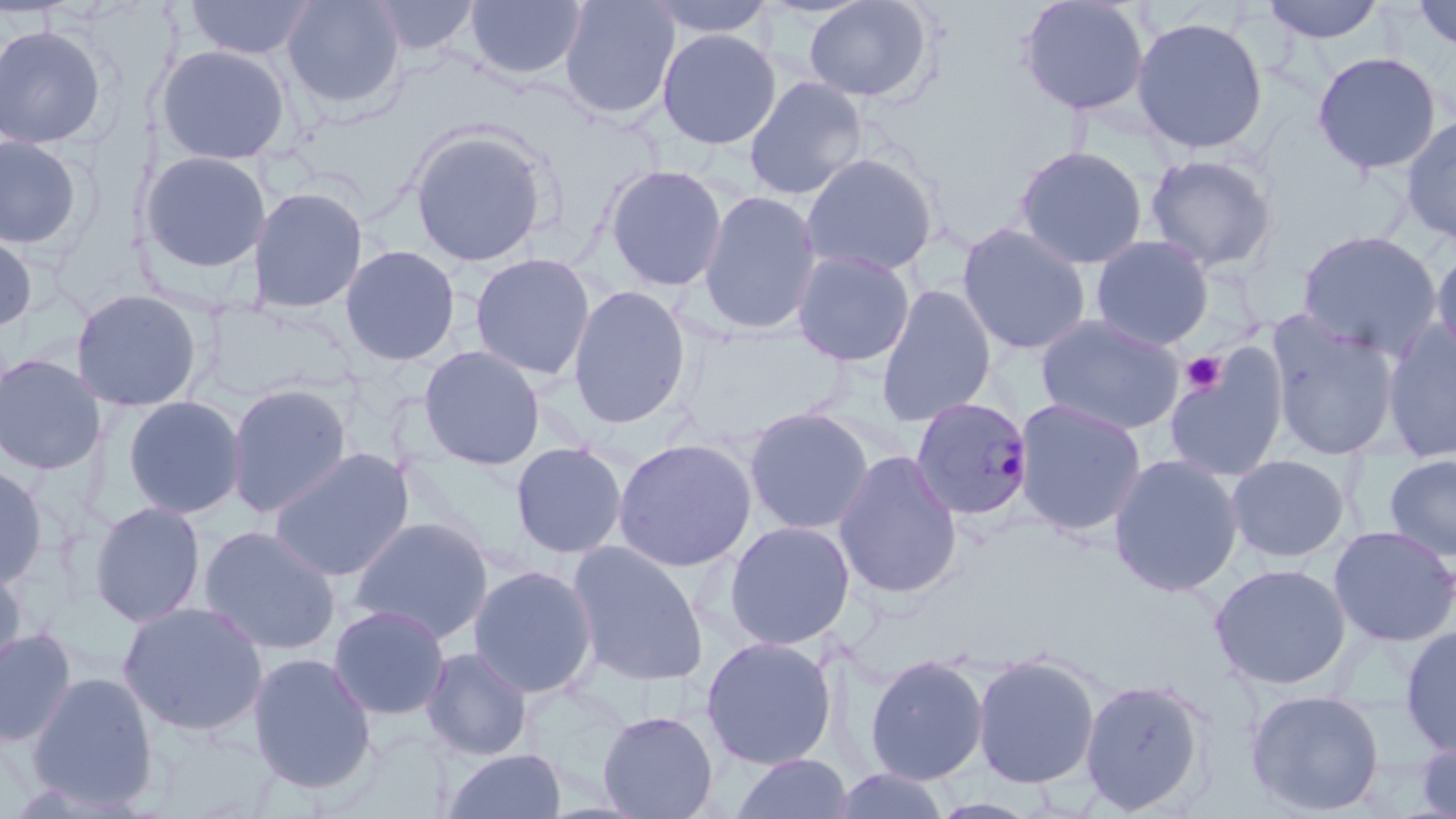
Summary:
  - Coordinate format: approximate bounding boxes as [x1, y1, x2, y2] in pixels
  - Platelet locations: [1181, 351, 1227, 395]
  - Plasmodium malariae-infected red blood cell locations: [910, 396, 1034, 521]
  - Uninfected red blood cell locations: [183, 0, 317, 60], [368, 0, 480, 56], [559, 0, 680, 120], [643, 0, 777, 39], [804, 0, 932, 103], [1018, 0, 1150, 116], [1261, 0, 1385, 44], [1412, 0, 1456, 53], [282, 1, 404, 110], [465, 1, 587, 81], [1131, 16, 1269, 154], [1, 24, 108, 149], [657, 28, 781, 149], [156, 44, 292, 165], [1312, 51, 1442, 174], [744, 76, 867, 200], [1400, 115, 1456, 247], [410, 128, 550, 267], [0, 135, 83, 250], [1014, 145, 1148, 270], [138, 150, 271, 274], [800, 153, 938, 277], [1145, 153, 1278, 273], [604, 164, 728, 291], [248, 185, 368, 314], [699, 191, 821, 335], [956, 223, 1092, 355], [1297, 230, 1442, 360], [0, 232, 37, 333], [1091, 235, 1213, 350], [1431, 243, 1456, 363], [339, 244, 461, 366], [792, 249, 916, 366], [469, 253, 596, 380], [876, 284, 996, 426], [568, 285, 691, 429], [71, 289, 205, 412], [1035, 314, 1185, 436], [1266, 314, 1401, 461], [1382, 322, 1456, 463], [1164, 343, 1289, 483], [419, 345, 545, 470], [0, 353, 105, 475], [226, 383, 352, 517], [122, 395, 247, 519], [1013, 398, 1147, 536], [744, 407, 874, 535], [613, 437, 757, 572], [510, 441, 628, 560], [268, 447, 415, 582], [833, 449, 963, 598], [1108, 453, 1244, 596], [1226, 454, 1350, 562], [1383, 454, 1456, 562], [0, 462, 48, 590], [89, 501, 206, 626], [348, 516, 495, 645], [724, 521, 855, 650], [198, 525, 341, 655], [1328, 525, 1456, 647], [567, 541, 708, 687], [1210, 563, 1351, 689], [0, 564, 27, 682], [467, 564, 599, 699], [117, 600, 269, 736], [327, 604, 450, 720], [1399, 625, 1456, 757], [0, 627, 77, 747], [700, 636, 837, 770], [421, 647, 532, 761], [247, 651, 377, 794], [971, 652, 1101, 789], [864, 653, 988, 785], [26, 672, 159, 809], [1079, 677, 1209, 815], [1244, 689, 1385, 816], [597, 709, 719, 819], [1416, 735, 1456, 819], [441, 748, 567, 819], [729, 753, 854, 818], [830, 768, 952, 819], [929, 796, 1045, 818]
  - Slide-level diagnosis: Plasmodium malariae
  - Modality: optical microscopy
  - Image size: 1456×819 pixels
  - Field of view: one of a larger specimen
  - Magnification: 1000x
  - Stain: May-Grünwald-Giemsa
  - Preparation: thin blood smear